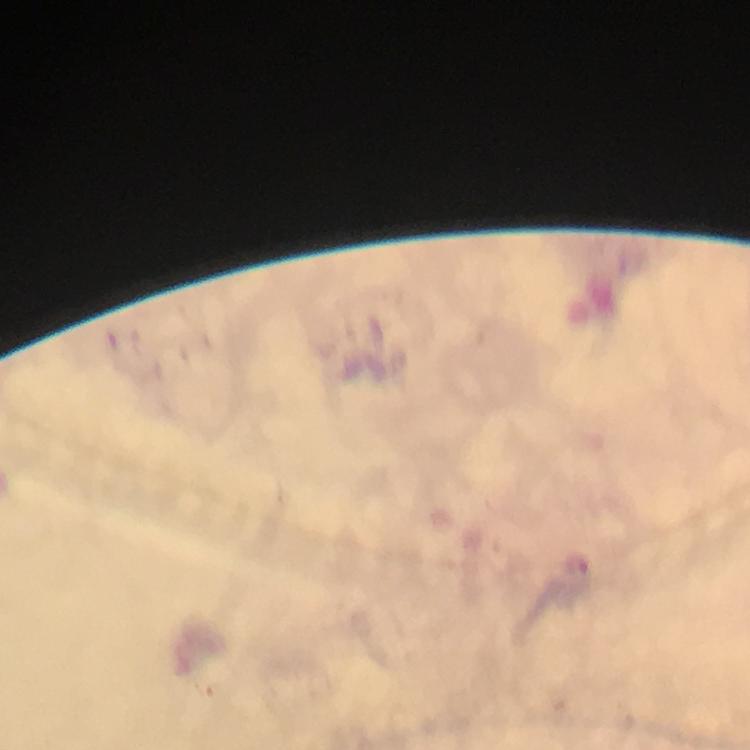

Approximate centers as [x, y] in pixels.
Summary:
  - Plasmodium parasite locations: [582, 571]
  - Magnification: 100x
  - Capture: smartphone mounted on the microscope
  - Preparation: thick blood smear
  - Cropped from: one field of view
  - Context: from a diagnostic examination for malaria
  - Stain: Giemsa
  - Immersion oil: applied
  - Image size: 750×750 pixels